Draw a bounding box around every leukocyte (white blood cell).
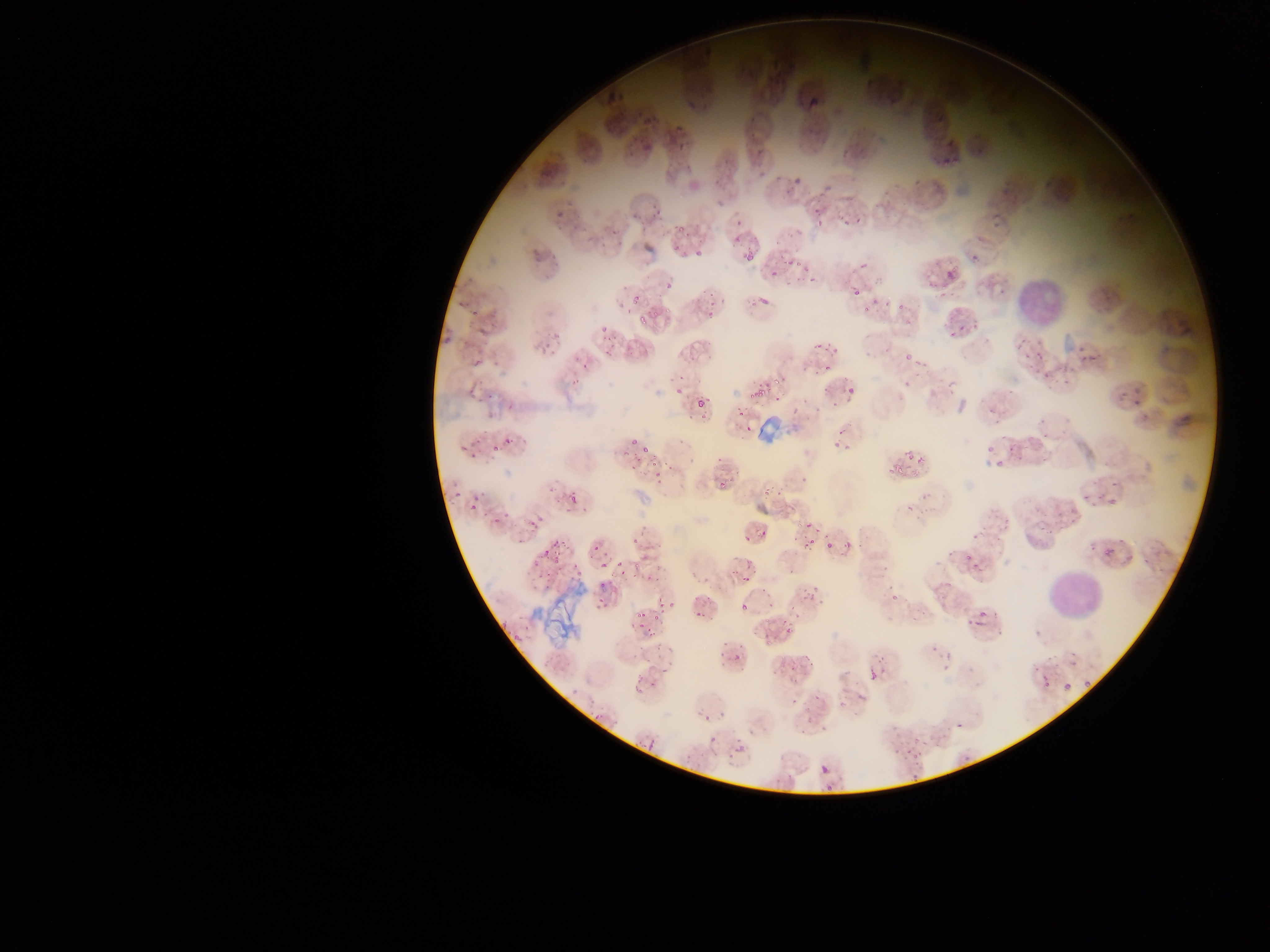

Approximate bounding boxes as (left, top, right, bottom) in pixels.
Leukocytes: (1013, 273, 1068, 325), (1053, 568, 1097, 620).

{
  "capture": "mobile-phone photograph through a microscope",
  "preparation": "thin blood smear",
  "image_size": "1270×952 pixels",
  "plasmodium_parasite_locations": "approximate bounding boxes as (left, top, right, bottom) in pixels: (695, 42, 716, 62), (765, 57, 792, 86), (600, 67, 645, 107), (804, 84, 827, 112), (671, 124, 694, 143), (638, 132, 660, 155), (938, 138, 962, 166), (786, 170, 808, 192), (629, 196, 659, 221), (552, 206, 569, 223), (808, 211, 821, 227), (839, 211, 864, 233), (729, 212, 742, 242), (671, 217, 694, 241), (599, 228, 618, 248), (531, 240, 552, 261), (675, 240, 694, 253), (638, 242, 653, 263), (969, 249, 985, 264), (740, 250, 758, 268), (688, 253, 706, 265), (769, 259, 790, 278), (798, 262, 814, 284), (942, 268, 960, 282), (661, 272, 680, 294), (923, 276, 943, 295), (845, 281, 866, 307), (746, 288, 773, 309), (869, 294, 880, 305), (633, 295, 644, 305), (467, 298, 491, 324), (895, 301, 904, 310), (619, 302, 628, 312), (704, 304, 718, 319), (633, 311, 655, 326), (947, 320, 967, 335), (439, 324, 460, 349), (538, 325, 565, 360), (593, 325, 614, 349), (644, 336, 662, 348), (900, 340, 917, 361), (1014, 341, 1039, 364), (814, 342, 822, 349), (473, 348, 492, 371), (1072, 350, 1092, 369), (570, 358, 588, 376), (770, 368, 788, 399), (1034, 368, 1055, 385), (747, 378, 770, 399), (931, 379, 949, 397), (900, 380, 909, 398), (1110, 383, 1129, 407), (828, 385, 858, 423), (674, 386, 684, 396), (1126, 393, 1148, 414), (792, 394, 810, 416), (696, 397, 706, 407), (983, 397, 1002, 419), (505, 402, 517, 413), (729, 410, 750, 419), (1039, 422, 1053, 445), (740, 423, 752, 438), (623, 430, 637, 445), (463, 435, 480, 457), (495, 435, 515, 455), (834, 438, 851, 452), (985, 444, 995, 457), (1006, 446, 1017, 468), (897, 447, 929, 465), (629, 448, 657, 469), (882, 462, 901, 483), (990, 462, 1007, 474), (650, 473, 676, 491), (714, 479, 732, 496), (440, 484, 468, 508), (762, 488, 777, 502), (1080, 490, 1099, 507), (566, 492, 579, 504), (1110, 499, 1118, 506), (468, 500, 479, 515), (995, 501, 1007, 529), (520, 508, 539, 539), (487, 509, 512, 530), (1057, 509, 1079, 528), (798, 517, 815, 533), (629, 518, 657, 549), (740, 521, 770, 541), (958, 530, 981, 565), (805, 537, 815, 547), (538, 538, 567, 565), (822, 539, 841, 557), (590, 542, 607, 555), (1101, 546, 1116, 559), (1104, 548, 1113, 557), (634, 556, 655, 580), (738, 557, 759, 569), (599, 561, 608, 571), (535, 572, 569, 594), (742, 576, 750, 585), (804, 577, 825, 603), (598, 579, 607, 592), (930, 579, 946, 591), (885, 586, 904, 603), (697, 588, 716, 618), (596, 596, 611, 614), (658, 597, 675, 622), (735, 597, 746, 613), (631, 604, 653, 633), (965, 608, 989, 630), (773, 609, 799, 635), (727, 642, 744, 663), (665, 645, 674, 654), (929, 646, 954, 670), (866, 654, 890, 682), (784, 655, 811, 676), (1069, 658, 1079, 667), (636, 665, 655, 689), (1036, 666, 1051, 688), (1083, 676, 1090, 685), (1063, 682, 1071, 690), (570, 688, 578, 697), (792, 688, 816, 716), (846, 689, 863, 708), (698, 711, 715, 726), (700, 733, 717, 756), (635, 734, 658, 754), (906, 739, 933, 767), (732, 742, 743, 753), (820, 765, 829, 774) | approximate (x, y) pixel centers of objects too small to bound: (959, 724)",
  "field_of_view": "single",
  "country": "Ghana"
}